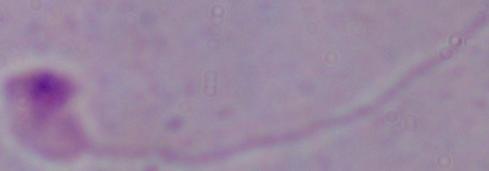
A Leishmania parasite is seen. Captured at 1000x magnification. Photomicrograph.